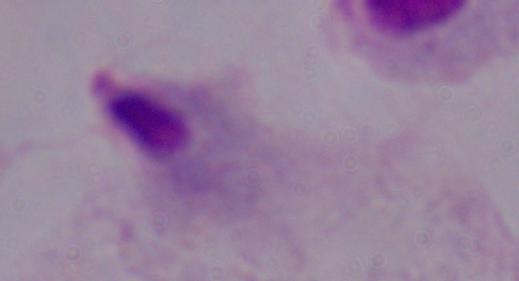

Summary:
  - Magnification: 1000x
  - Modality: micrograph
  - Identification: trichomonad